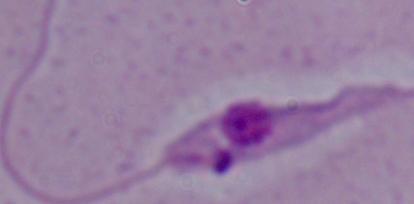
A Leishmania parasite is shown. Photomicrograph. 1000x magnification.